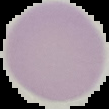
Summary:
  - Image size: 109×109 pixels
  - Image type: cell region segmented out of the field of view; surrounding area masked to black
  - Preparation: thin blood smear
  - Malaria status: uninfected